Assess this cell for malaria.
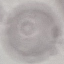

Uninfected.

Acquired by smartphone through the microscope eyepiece. Automatically extracted cell patch, resized to 64 × 64 pixels. Giemsa stain. Thin smear of blood.